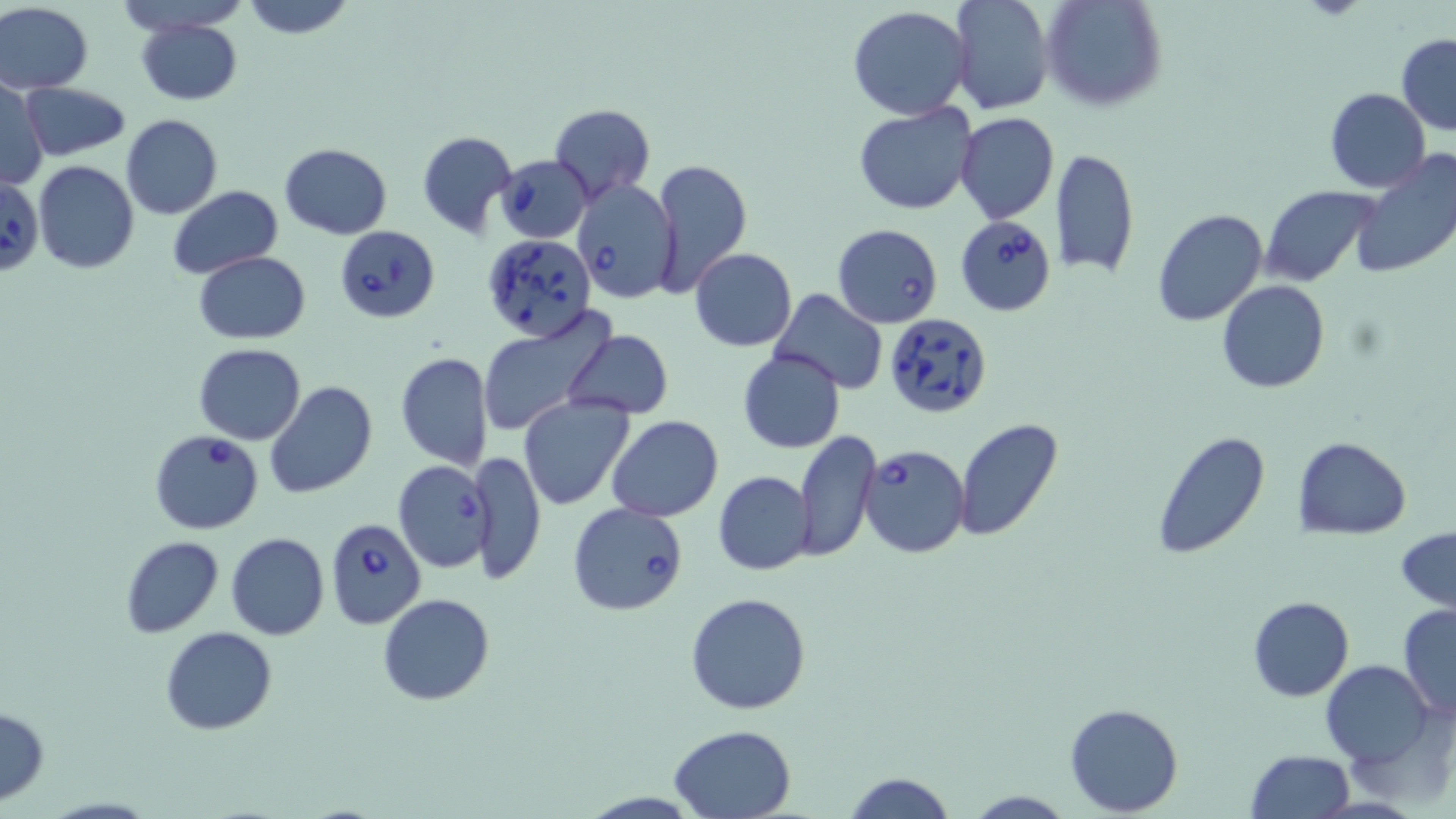

Approximate bounding boxes as named x1/y1/x2/y2 corners in pixels. Uninfected red blood cell locations: (x1=117, y1=0, x2=251, y2=34), (x1=241, y1=0, x2=356, y2=39), (x1=950, y1=0, x2=1053, y2=114), (x1=1038, y1=0, x2=1168, y2=112), (x1=0, y1=3, x2=93, y2=92), (x1=846, y1=5, x2=972, y2=122), (x1=136, y1=18, x2=242, y2=105), (x1=1397, y1=33, x2=1456, y2=135), (x1=0, y1=78, x2=48, y2=191), (x1=21, y1=82, x2=132, y2=159), (x1=1324, y1=88, x2=1432, y2=193), (x1=853, y1=102, x2=979, y2=217), (x1=547, y1=104, x2=655, y2=202), (x1=955, y1=112, x2=1059, y2=224), (x1=121, y1=113, x2=223, y2=219), (x1=416, y1=129, x2=517, y2=238), (x1=280, y1=142, x2=392, y2=238), (x1=1052, y1=147, x2=1139, y2=280), (x1=1350, y1=149, x2=1456, y2=279), (x1=649, y1=156, x2=752, y2=298), (x1=33, y1=161, x2=139, y2=274), (x1=1258, y1=184, x2=1377, y2=287), (x1=167, y1=185, x2=283, y2=279), (x1=1153, y1=210, x2=1268, y2=328), (x1=833, y1=223, x2=942, y2=328), (x1=689, y1=249, x2=797, y2=350), (x1=194, y1=251, x2=310, y2=344), (x1=1216, y1=281, x2=1331, y2=392), (x1=768, y1=289, x2=888, y2=396), (x1=478, y1=311, x2=610, y2=437), (x1=563, y1=330, x2=674, y2=419), (x1=194, y1=344, x2=306, y2=444), (x1=736, y1=349, x2=846, y2=454), (x1=395, y1=353, x2=492, y2=470), (x1=263, y1=380, x2=378, y2=500), (x1=519, y1=395, x2=633, y2=510), (x1=608, y1=416, x2=724, y2=522), (x1=954, y1=421, x2=1062, y2=541), (x1=1150, y1=428, x2=1272, y2=560), (x1=794, y1=429, x2=881, y2=562), (x1=1294, y1=436, x2=1410, y2=539), (x1=469, y1=451, x2=546, y2=582), (x1=714, y1=470, x2=815, y2=575), (x1=1397, y1=526, x2=1456, y2=616), (x1=225, y1=531, x2=331, y2=640), (x1=120, y1=536, x2=224, y2=638), (x1=686, y1=592, x2=812, y2=715), (x1=377, y1=594, x2=494, y2=706), (x1=1247, y1=595, x2=1354, y2=701), (x1=1396, y1=604, x2=1456, y2=720), (x1=159, y1=626, x2=278, y2=735), (x1=1321, y1=660, x2=1435, y2=767), (x1=1063, y1=702, x2=1184, y2=816), (x1=0, y1=704, x2=47, y2=806), (x1=669, y1=723, x2=797, y2=818), (x1=1246, y1=749, x2=1356, y2=819), (x1=840, y1=770, x2=957, y2=818), (x1=963, y1=790, x2=1075, y2=818). Babesia divergens-infected red blood cell locations: (x1=496, y1=154, x2=592, y2=243), (x1=1, y1=174, x2=43, y2=278), (x1=572, y1=179, x2=680, y2=303), (x1=955, y1=214, x2=1057, y2=316), (x1=334, y1=224, x2=439, y2=323), (x1=481, y1=231, x2=599, y2=341), (x1=884, y1=311, x2=993, y2=420), (x1=149, y1=430, x2=263, y2=534), (x1=859, y1=444, x2=971, y2=560), (x1=392, y1=460, x2=492, y2=574), (x1=569, y1=502, x2=690, y2=618), (x1=325, y1=516, x2=427, y2=630). Slide-level diagnosis: Babesia divergens. May-Grünwald-Giemsa-stained preparation. Light microscopy. Image is 1456×819 pixels. Single field of view. Captured at 1000x magnification. Thin blood smear.